Assess the morphology of the erythrocytes.
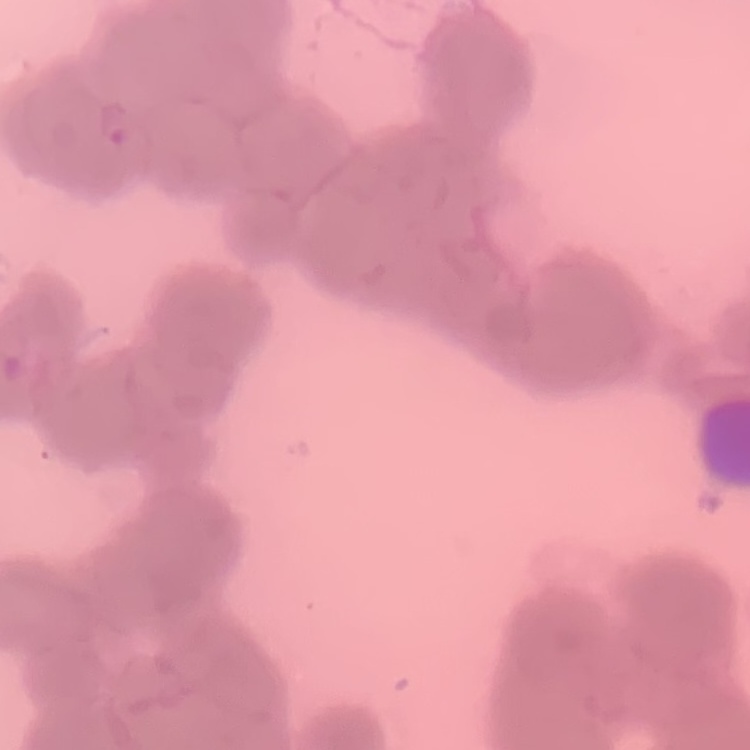

They show rouleaux formation.

preparation = thin blood film
image type = square crop of a larger photomicrograph
stain = Field's or Giemsa